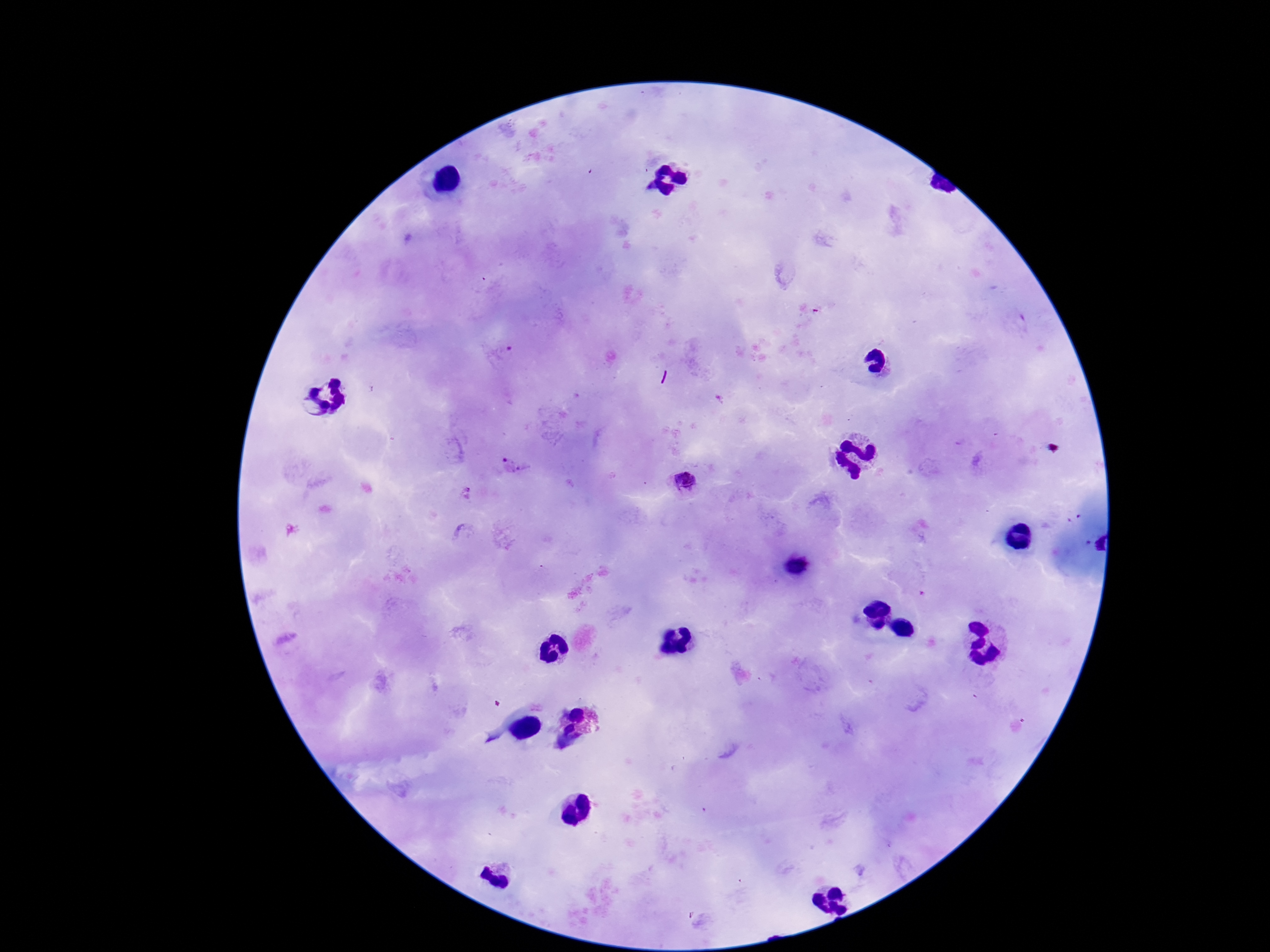
preparation = thick peripheral-blood smear
field of view = one from this slide
Plasmodium parasite locations = approximate centers as (x, y) in pixels: (496, 352), (512, 465), (684, 484), (466, 492)
capture = smartphone camera through the microscope eyepiece
image size = 1270×952 pixels
patient malaria status = positive
stain = Giemsa
magnification = 100x